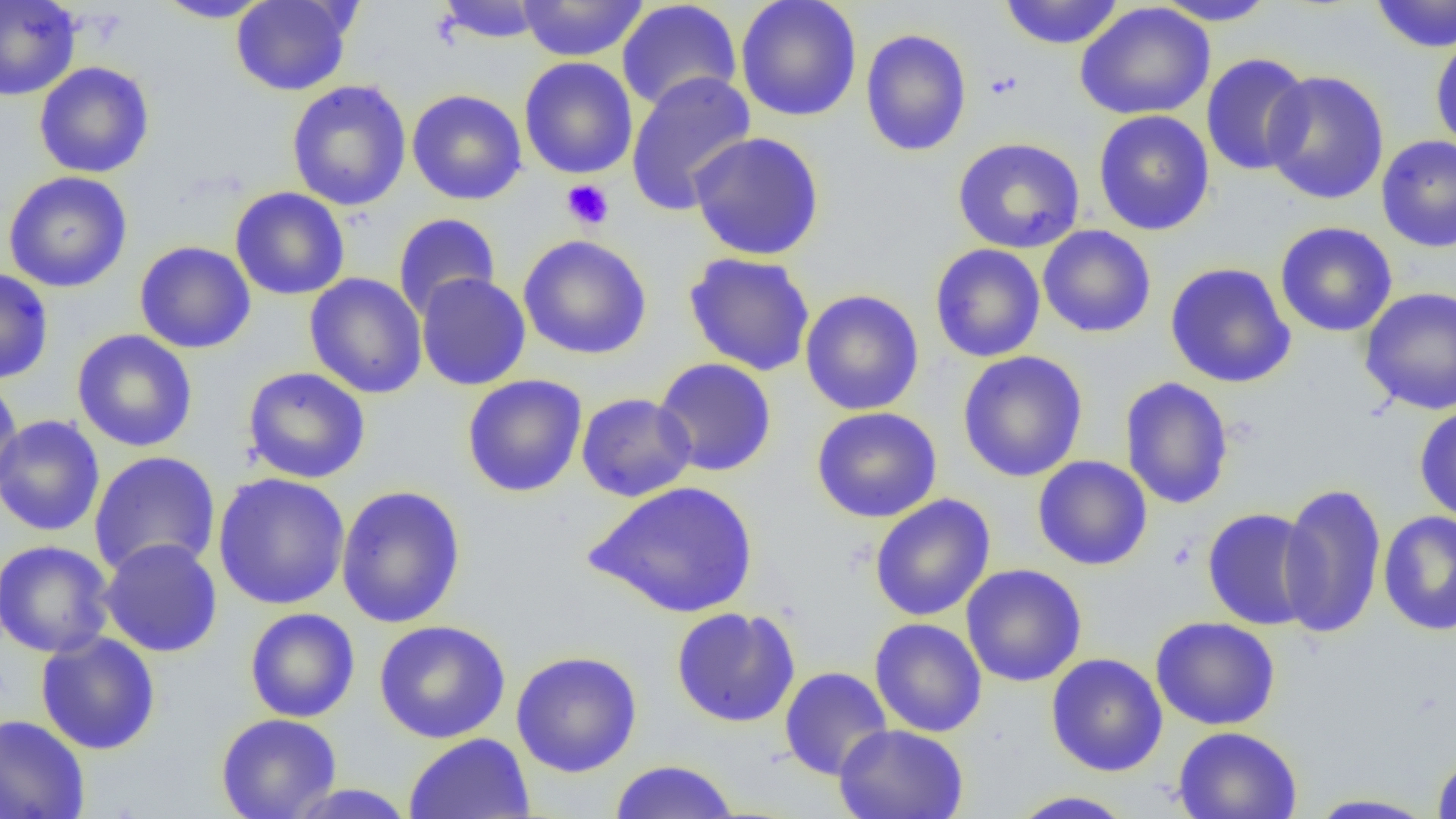

Summary:
  - Coordinate format: approximate bounding boxes as (x1, y1, x2, y2) in pixels
  - Uninfected red blood cell locations: (0, 0, 81, 101), (155, 0, 275, 23), (230, 0, 356, 96), (435, 0, 547, 44), (735, 0, 862, 121), (998, 0, 1125, 50), (1369, 0, 1456, 53), (517, 1, 648, 62), (616, 1, 743, 111), (1153, 1, 1280, 27), (1075, 3, 1215, 120), (859, 29, 973, 156), (1430, 31, 1456, 156), (1201, 53, 1314, 176), (519, 57, 638, 179), (33, 62, 154, 178), (626, 70, 757, 216), (1262, 70, 1390, 206), (286, 80, 412, 211), (406, 89, 527, 205), (1093, 110, 1215, 236), (687, 131, 826, 260), (1376, 135, 1456, 253), (952, 137, 1085, 254), (3, 171, 133, 293), (230, 187, 350, 300), (392, 213, 500, 318), (1275, 221, 1398, 338), (1037, 225, 1156, 338), (518, 234, 653, 360), (134, 240, 256, 354), (929, 244, 1046, 363), (683, 252, 816, 377), (1165, 262, 1297, 388), (0, 268, 54, 384), (304, 272, 428, 399), (415, 273, 531, 391), (1359, 286, 1456, 415), (800, 289, 925, 416), (71, 329, 198, 452), (957, 350, 1089, 483), (652, 358, 777, 477), (242, 367, 371, 484), (462, 374, 588, 497), (0, 377, 24, 497), (1119, 377, 1235, 509), (576, 392, 697, 502), (1414, 404, 1456, 524), (811, 406, 942, 523), (0, 415, 105, 537), (88, 450, 221, 578), (1032, 455, 1153, 571), (212, 472, 350, 611), (582, 480, 760, 618), (1277, 481, 1387, 640), (336, 484, 466, 629), (869, 494, 996, 621), (1202, 507, 1319, 630), (1378, 511, 1455, 636), (98, 538, 223, 658), (0, 539, 115, 658), (961, 564, 1087, 687), (670, 606, 801, 727), (244, 607, 360, 723), (1150, 616, 1281, 731), (869, 617, 987, 737), (373, 620, 511, 744), (35, 631, 161, 755), (510, 650, 643, 777), (1046, 653, 1169, 777), (779, 666, 893, 781), (0, 713, 90, 819), (215, 713, 342, 819), (833, 724, 968, 819), (1172, 726, 1303, 819), (403, 732, 536, 819), (1432, 753, 1456, 818), (608, 759, 740, 818), (282, 784, 417, 818), (1007, 790, 1139, 818), (1305, 793, 1439, 818)
  - Platelet locations: (983, 70, 1024, 101), (561, 179, 614, 230)
  - Slide-level diagnosis: no evidence of blood parasites
  - Image size: 1456×819 pixels
  - Magnification: 1000x
  - Field of view: one of a larger specimen
  - Modality: light microscopy
  - Preparation: thin blood film